Locate and identify every blood parasite.
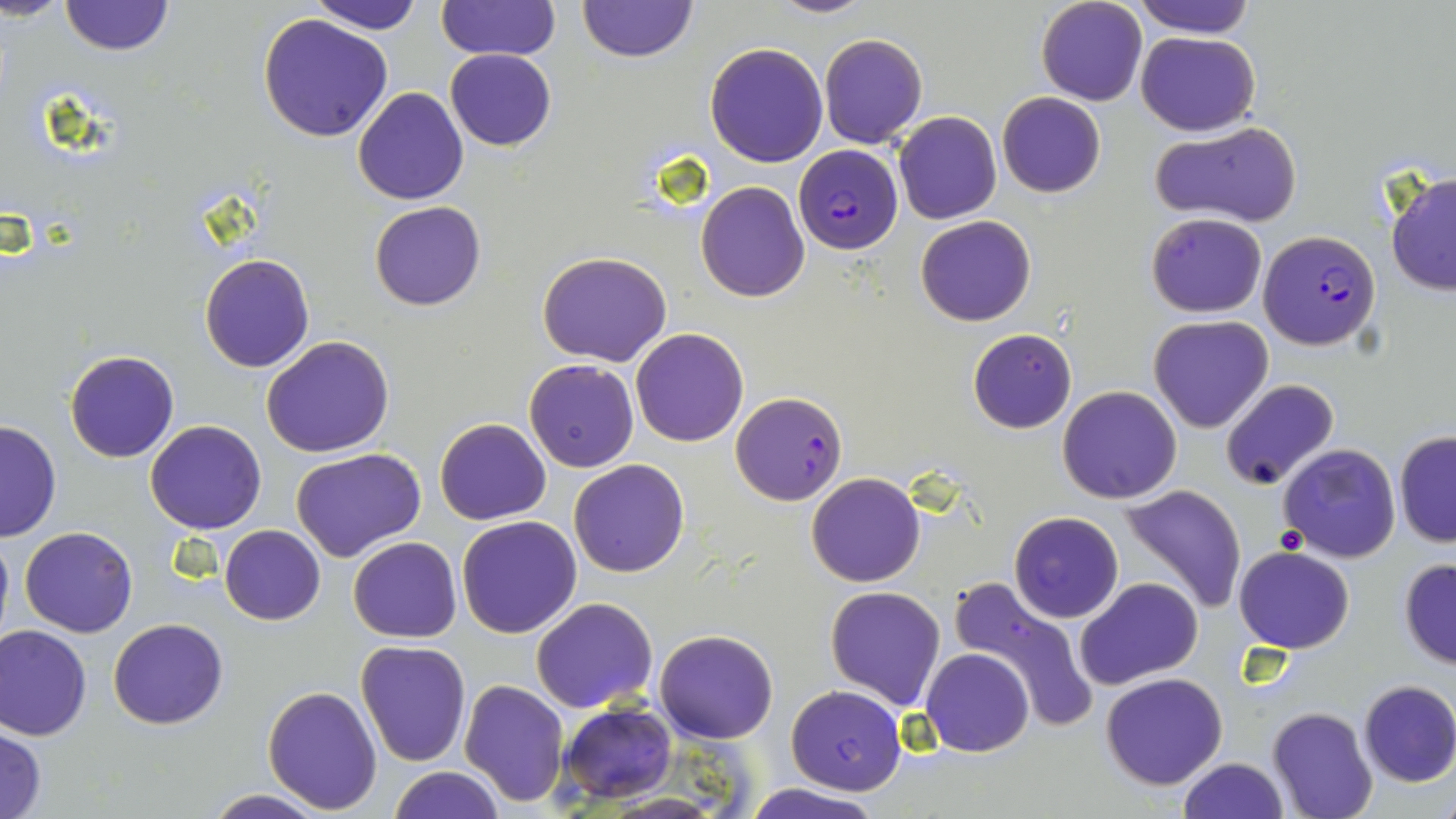
Approximate bounding boxes as [x1, y1, x2, y2] in pixels.
Plasmodium falciparum-infected red blood cells: [793, 143, 903, 253], [1257, 229, 1382, 350], [729, 391, 848, 505].
No Plasmodium ovale, Plasmodium malariae, Plasmodium vivax, Babesia divergens, or Trypanosoma brucei observed.

Uninfected red blood cell locations: [577, 0, 695, 62], [767, 0, 875, 18], [1036, 0, 1146, 105], [1132, 0, 1257, 38], [57, 1, 174, 57], [306, 1, 424, 34], [437, 1, 560, 64], [258, 12, 394, 142], [1136, 30, 1260, 137], [820, 33, 927, 149], [705, 42, 829, 167], [444, 48, 557, 151], [353, 87, 469, 205], [997, 92, 1106, 198], [894, 112, 1002, 224], [1151, 119, 1304, 229], [1384, 171, 1456, 296], [696, 181, 811, 302], [370, 201, 486, 311], [1146, 213, 1267, 317], [915, 214, 1037, 327], [537, 251, 672, 367], [200, 254, 314, 373], [1148, 316, 1273, 434], [968, 327, 1076, 433], [629, 328, 748, 447], [262, 335, 395, 458], [65, 350, 179, 462], [524, 358, 639, 472], [1220, 378, 1341, 491], [1058, 386, 1182, 503], [1242, 409, 1375, 551], [435, 418, 552, 525], [0, 419, 61, 542], [144, 419, 268, 534], [1394, 430, 1456, 547], [1277, 444, 1402, 565], [290, 447, 427, 563], [568, 458, 691, 577], [806, 472, 926, 587], [1117, 483, 1248, 614], [1008, 512, 1123, 623], [456, 516, 582, 638], [0, 523, 14, 649], [220, 524, 326, 625], [20, 526, 138, 638], [349, 536, 462, 641], [1234, 546, 1355, 653], [1398, 558, 1456, 670], [945, 573, 1100, 735], [1074, 578, 1203, 690], [825, 586, 946, 710], [531, 597, 658, 713], [108, 617, 229, 729], [0, 624, 93, 740], [654, 629, 779, 743], [354, 640, 472, 768], [922, 648, 1034, 758], [1100, 673, 1228, 791], [458, 678, 569, 807], [1357, 681, 1456, 788], [262, 685, 382, 813], [785, 685, 907, 795], [555, 701, 677, 804], [1267, 705, 1378, 819], [0, 726, 48, 819], [1178, 756, 1288, 819], [385, 767, 506, 819], [743, 783, 882, 819], [201, 790, 333, 819]. Slide-level diagnosis: Plasmodium falciparum. Light microscopy. Thin blood film. Captured at 1000x magnification. Image is 1456×819 pixels. One field of a larger specimen. May-Grünwald-Giemsa-stained preparation.